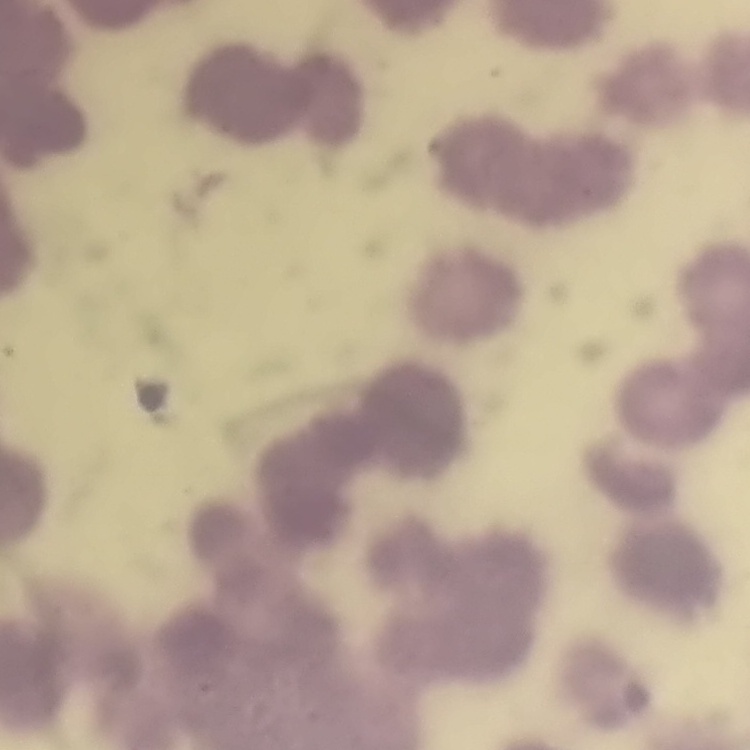

The erythrocytes show rouleaux formation. Thin blood film. Stained with either Field's or Giemsa. One tile cut from a larger photomicrograph.